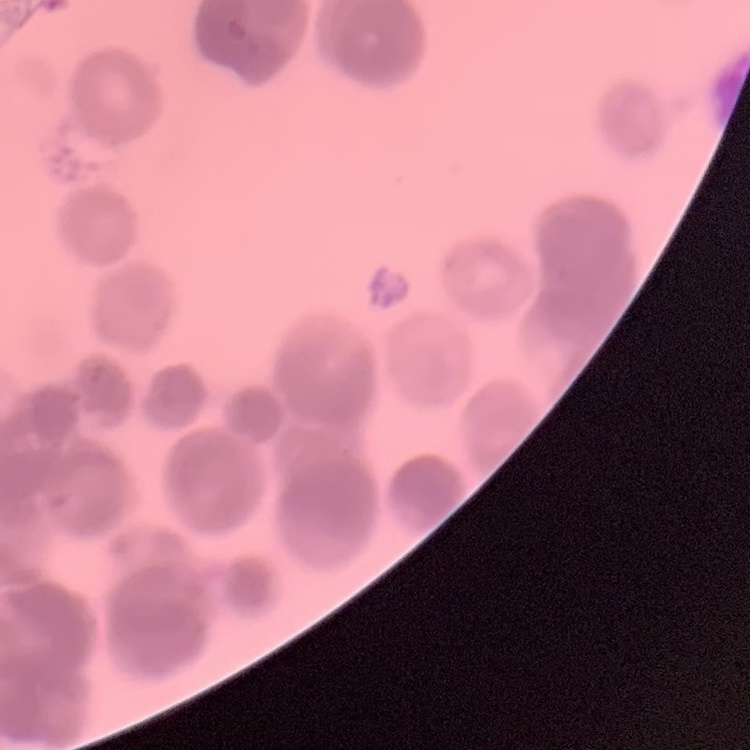

red blood cell morphology = rouleaux formation
image type = one tile cut from a larger photomicrograph
stain = Field's or Giemsa
preparation = thin blood film